State which parasite is depicted.
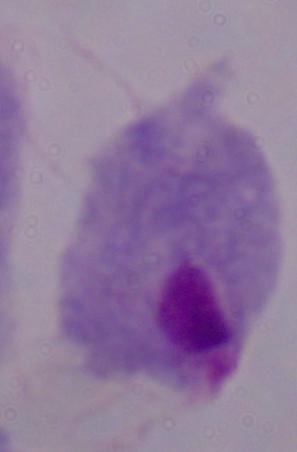

This is a trichomonad.

modality = micrograph
magnification = 1000x